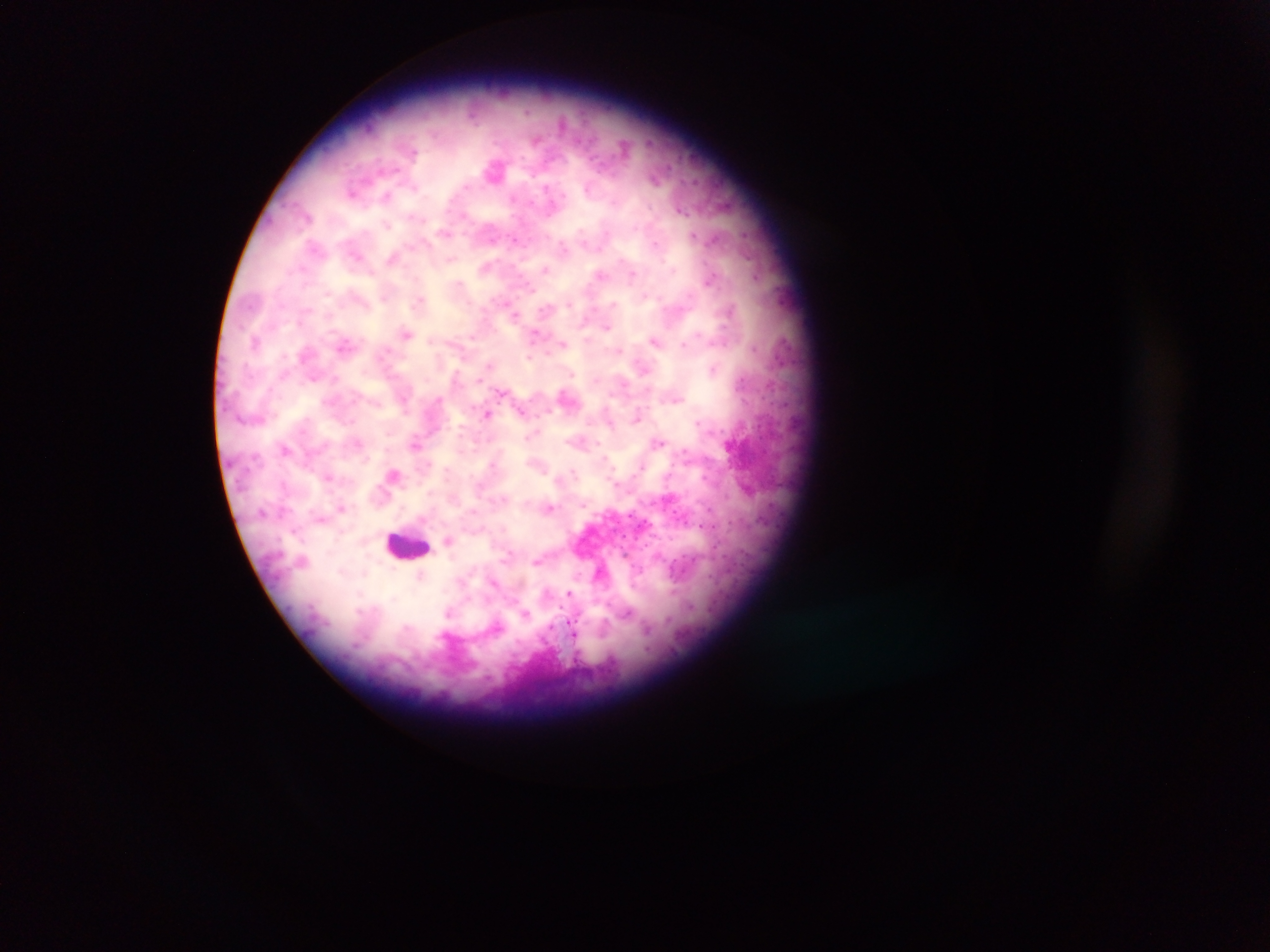

Approximate centers as {x, y} in pixels.
Summary:
  - Malaria parasite locations: {494, 169}, {415, 188}, {546, 188}, {387, 197}, {512, 198}, {308, 216}, {414, 217}, {387, 226}, {745, 233}, {693, 235}, {514, 239}, {655, 243}, {563, 247}, {357, 256}, {392, 257}, {449, 261}, {301, 268}, {546, 269}, {600, 275}, {633, 275}, {710, 281}, {459, 283}, {532, 290}, {645, 296}, {384, 297}, {419, 301}, {612, 303}, {570, 304}, {511, 309}, {515, 316}, {607, 327}, {534, 333}, {405, 334}, {255, 341}, {655, 341}, {562, 343}, {343, 344}, {684, 345}, {754, 347}, {620, 350}, {385, 352}, {530, 357}, {643, 368}, {713, 369}, {572, 374}, {313, 379}, {336, 379}, {479, 379}, {500, 392}, {675, 399}, {521, 411}, {548, 411}, {486, 414}, {637, 416}, {698, 421}, {610, 423}, {531, 435}, {357, 442}, {597, 442}, {659, 442}, {415, 443}, {285, 449}, {685, 452}, {605, 458}, {491, 463}, {428, 464}, {640, 468}, {573, 471}, {394, 474}, {328, 477}, {284, 485}, {504, 498}, {583, 505}, {341, 507}, {550, 507}, {449, 540}, {510, 553}, {536, 561}, {420, 576}, {495, 583}, {569, 593}, {449, 612}, {526, 614}, {571, 629}
  - Leukocyte locations: {408, 545}
  - Field of view: single
  - Image size: 1270×952 pixels
  - Country: Ghana
  - Capture: mobile-phone photograph through a microscope
  - Preparation: thick blood film